Report the malaria status of this cell.
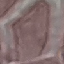

Uninfected.

Thin blood smear. Automatically extracted cell patch, resized to 64 × 64 pixels. Giemsa stain. Photographed with a smartphone camera at the microscope eyepiece.